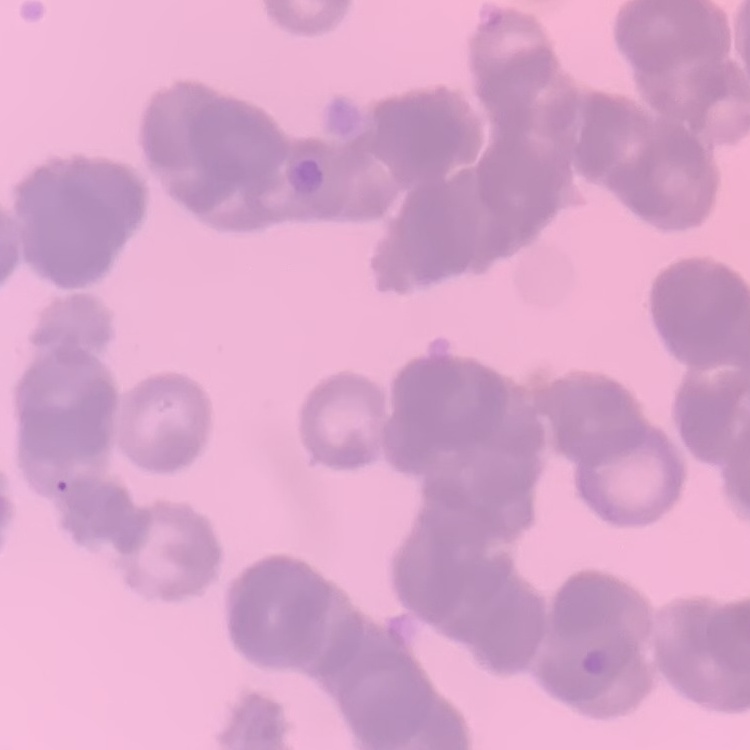
{
  "red_blood_cell_morphology": "rouleaux formation",
  "stain": "Field's or Giemsa",
  "preparation": "thin blood smear",
  "image_type": "one tile cut from a larger photomicrograph"
}